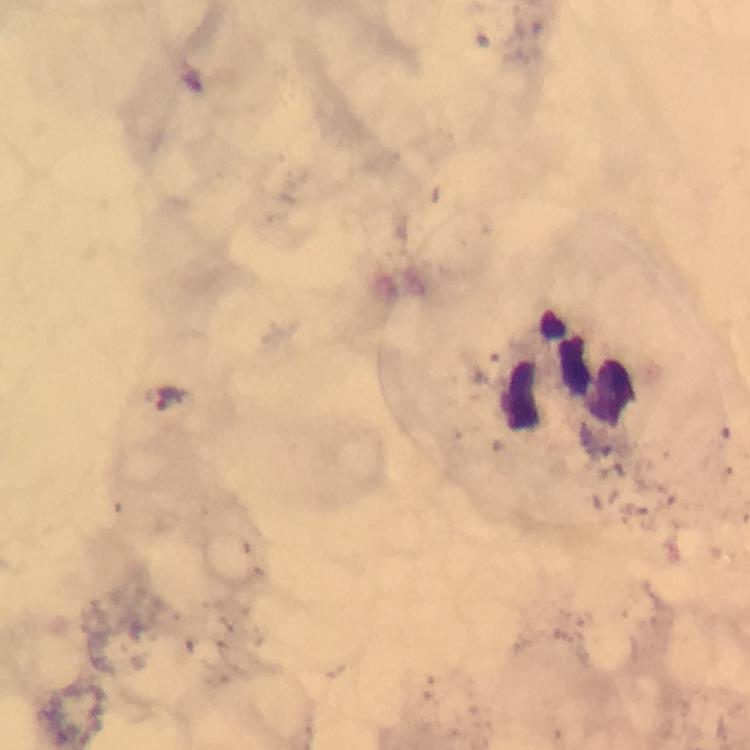
Plasmodium parasites = none detected
image size = 750×750 pixels
leukocyte locations = approximate centers as [x, y] in pixels: [571, 370]
magnification = 100x
context = from a diagnostic examination for malaria
preparation = thick smear
cropped from = a single field of view
immersion oil = used
capture = smartphone mounted on the microscope
stain = Giemsa